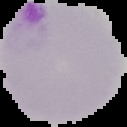
image type = cell region segmented out of the field of view; surrounding area masked to black
preparation = thin blood smear
malaria status = parasitized
image size = 127×127 pixels